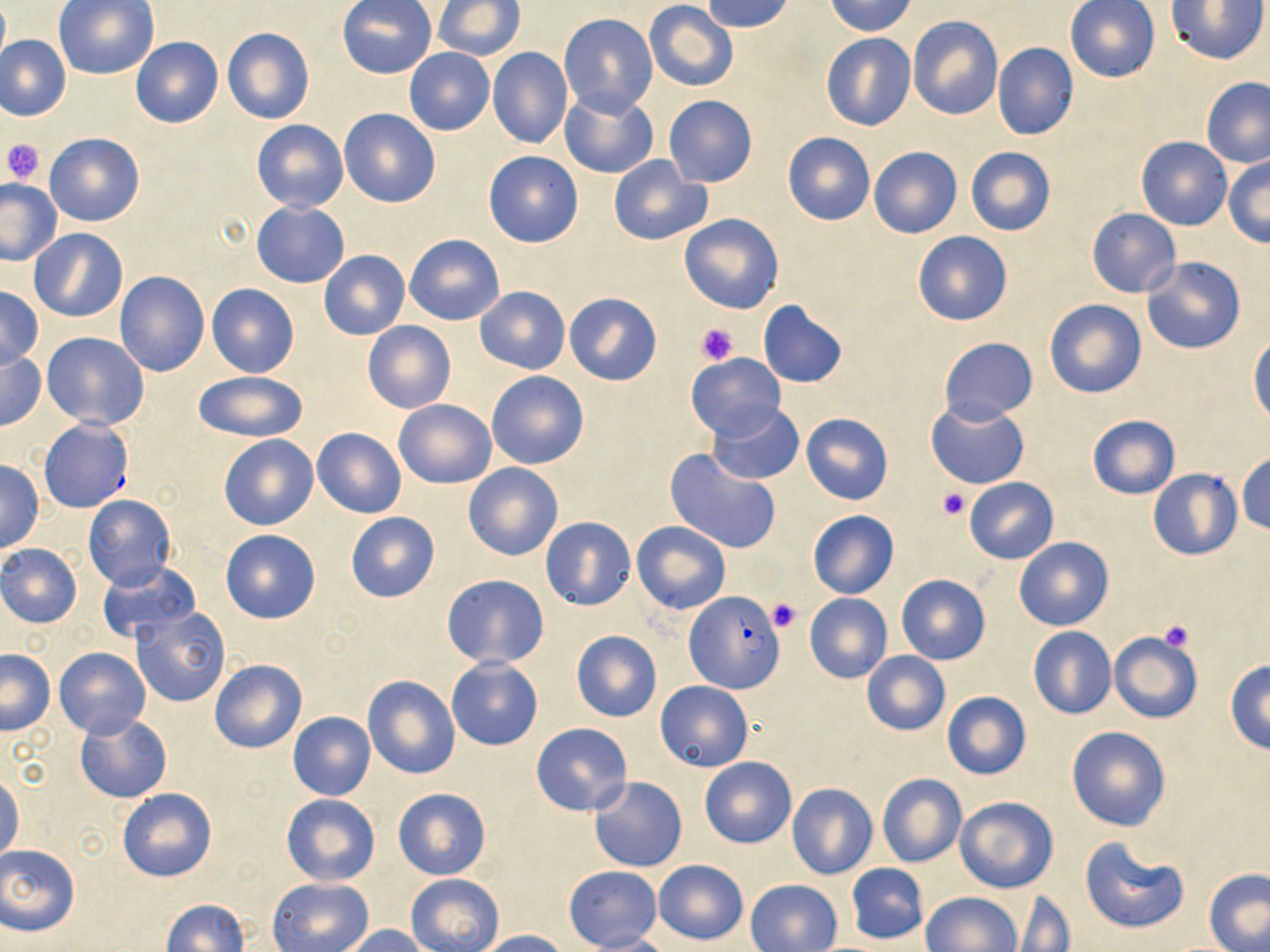
slide-level diagnosis = Plasmodium falciparum
magnification = 1000x
image size = 1270×952 pixels
platelet locations = approximate bounding boxes as (x1, y1, x2, y2) in pixels: (1, 138, 44, 184), (695, 322, 740, 365), (937, 486, 970, 520), (767, 598, 799, 631), (1159, 619, 1195, 653)
Plasmodium falciparum-infected red blood cell locations = approximate bounding boxes as (x1, y1, x2, y2) in pixels: (684, 590, 784, 694)
uninfected red blood cell locations = approximate bounding boxes as (x1, y1, x2, y2) in pixels: (1166, 0, 1268, 67), (0, 1, 10, 71), (53, 1, 158, 79), (337, 1, 436, 79), (433, 1, 525, 60), (700, 1, 796, 33), (823, 1, 917, 37), (1065, 1, 1160, 82), (644, 2, 738, 91), (558, 14, 659, 117), (907, 16, 1003, 120), (222, 27, 315, 124), (820, 34, 916, 131), (0, 35, 72, 121), (131, 36, 223, 128), (992, 43, 1078, 140), (404, 48, 495, 135), (487, 48, 573, 150), (1200, 77, 1270, 168), (560, 90, 658, 181), (665, 96, 757, 187), (338, 108, 441, 208), (251, 119, 348, 212), (44, 132, 144, 226), (782, 132, 875, 225), (1137, 136, 1232, 230), (965, 146, 1056, 237), (868, 147, 963, 239), (483, 150, 583, 247), (607, 154, 710, 246), (1224, 154, 1270, 247), (0, 177, 64, 265), (251, 202, 350, 288), (1085, 208, 1180, 298), (678, 213, 784, 314), (28, 228, 128, 321), (913, 230, 1012, 325), (405, 233, 505, 325), (318, 250, 411, 341), (1141, 256, 1246, 354), (115, 271, 210, 376), (206, 283, 299, 377), (0, 286, 42, 368), (475, 287, 570, 374), (565, 292, 662, 385), (1044, 299, 1146, 398), (757, 300, 849, 388), (362, 321, 455, 414), (43, 333, 149, 428), (1248, 335, 1270, 426), (939, 337, 1037, 424), (1, 349, 45, 431), (686, 353, 786, 442), (486, 369, 589, 470), (192, 372, 309, 443), (394, 399, 497, 488), (925, 400, 1030, 489), (707, 405, 806, 484), (800, 412, 892, 505), (1086, 414, 1179, 499), (39, 419, 133, 513), (312, 428, 406, 518), (218, 433, 320, 531), (666, 448, 781, 555), (1236, 452, 1270, 535), (0, 459, 44, 553), (463, 462, 563, 561), (1148, 469, 1240, 560), (964, 477, 1058, 564), (83, 494, 176, 592), (807, 510, 899, 598), (345, 513, 440, 602), (541, 516, 636, 611), (632, 521, 730, 614), (220, 528, 322, 623), (1014, 536, 1113, 630), (0, 543, 82, 628), (96, 562, 202, 643), (442, 574, 549, 669), (896, 574, 990, 664), (804, 593, 893, 683), (132, 608, 230, 708), (1027, 627, 1116, 718), (570, 631, 661, 722), (1109, 631, 1202, 724), (55, 647, 150, 738), (0, 650, 56, 734), (861, 651, 951, 736), (210, 658, 306, 754), (446, 658, 543, 750), (1224, 660, 1270, 752), (361, 675, 460, 779), (656, 680, 752, 771), (941, 690, 1030, 780), (288, 712, 377, 801), (73, 713, 172, 804), (531, 722, 633, 816), (1066, 726, 1171, 832), (699, 756, 797, 849), (1, 770, 23, 864), (876, 773, 967, 868), (590, 777, 687, 872), (787, 782, 877, 879), (117, 787, 217, 883), (393, 788, 490, 880), (282, 794, 380, 886), (954, 796, 1059, 893), (1078, 836, 1190, 936), (0, 844, 81, 936), (654, 859, 748, 944), (846, 863, 929, 944), (564, 866, 663, 950), (1204, 868, 1270, 951), (407, 874, 502, 952), (267, 878, 373, 951), (746, 879, 842, 952), (1011, 891, 1075, 951), (923, 892, 1022, 952), (159, 899, 250, 952), (338, 924, 433, 952), (479, 930, 571, 952), (577, 933, 673, 951)
stain = May-Grünwald-Giemsa
modality = light microscopy
preparation = thin blood film
field of view = single